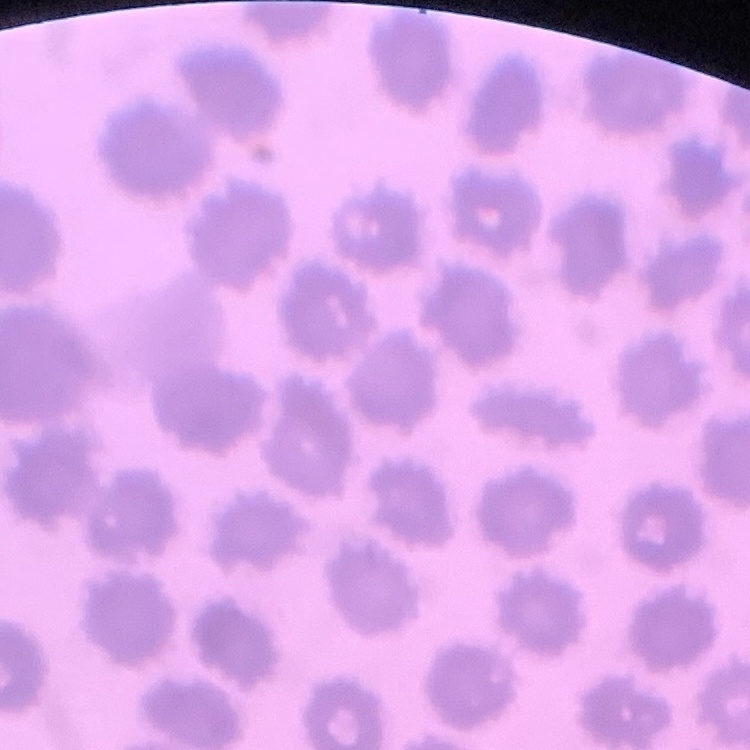
Summary:
  - Red blood cell morphology: no rouleaux formation
  - Preparation: thin blood smear
  - Image type: square crop of a larger photomicrograph
  - Stain: Field's or Giemsa